Locate every blood parasite and identify its species.
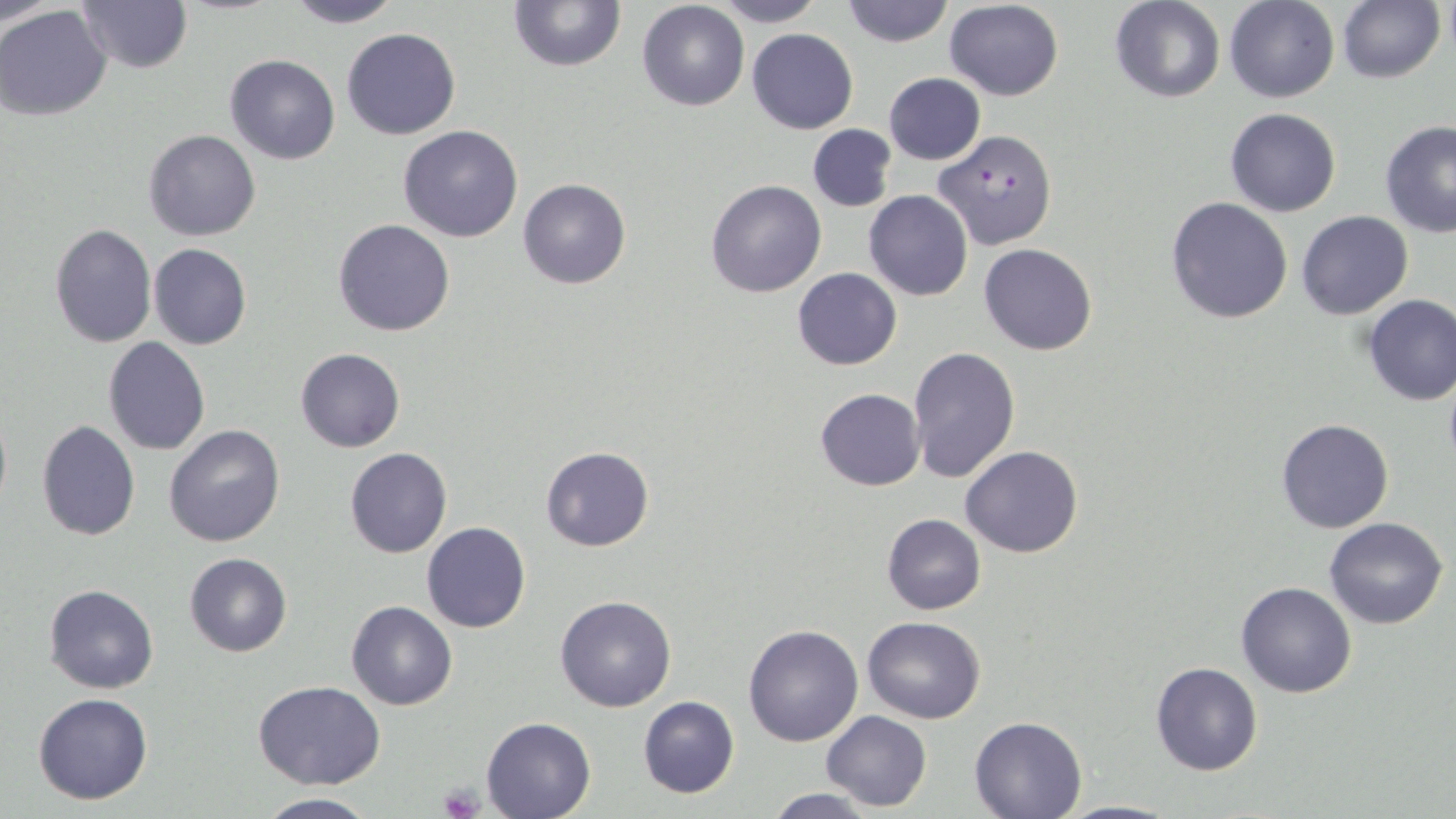

Approximate bounding boxes as named x1/y1/x2/y2 corners in pixels.
Plasmodium falciparum-infected red blood cells: (x1=934, y1=130, x2=1058, y2=249).
No Plasmodium ovale, Plasmodium malariae, Plasmodium vivax, Babesia divergens, or Trypanosoma brucei observed.

Summary:
  - Uninfected red blood cell locations: (x1=1, y1=0, x2=61, y2=29), (x1=280, y1=0, x2=404, y2=28), (x1=507, y1=0, x2=626, y2=71), (x1=712, y1=0, x2=824, y2=27), (x1=839, y1=0, x2=954, y2=48), (x1=1110, y1=0, x2=1224, y2=103), (x1=1225, y1=0, x2=1339, y2=102), (x1=77, y1=1, x2=193, y2=75), (x1=944, y1=1, x2=1063, y2=100), (x1=637, y1=2, x2=748, y2=112), (x1=1336, y1=2, x2=1445, y2=84), (x1=0, y1=5, x2=113, y2=122), (x1=341, y1=27, x2=460, y2=140), (x1=747, y1=28, x2=858, y2=132), (x1=224, y1=54, x2=340, y2=164), (x1=883, y1=72, x2=985, y2=164), (x1=1224, y1=107, x2=1342, y2=217), (x1=1379, y1=121, x2=1456, y2=238), (x1=807, y1=124, x2=897, y2=212), (x1=397, y1=125, x2=525, y2=242), (x1=142, y1=129, x2=263, y2=242), (x1=518, y1=178, x2=631, y2=289), (x1=705, y1=180, x2=825, y2=298), (x1=864, y1=190, x2=972, y2=301), (x1=1166, y1=197, x2=1293, y2=324), (x1=1298, y1=211, x2=1412, y2=320), (x1=334, y1=219, x2=455, y2=336), (x1=49, y1=224, x2=157, y2=347), (x1=149, y1=244, x2=252, y2=350), (x1=978, y1=244, x2=1097, y2=355), (x1=793, y1=267, x2=901, y2=369), (x1=1361, y1=294, x2=1456, y2=407), (x1=103, y1=337, x2=211, y2=455), (x1=906, y1=346, x2=1022, y2=484), (x1=294, y1=348, x2=406, y2=453), (x1=1443, y1=374, x2=1456, y2=477), (x1=814, y1=389, x2=924, y2=491), (x1=0, y1=402, x2=11, y2=520), (x1=1275, y1=417, x2=1394, y2=534), (x1=35, y1=420, x2=140, y2=540), (x1=165, y1=425, x2=285, y2=548), (x1=961, y1=445, x2=1083, y2=558), (x1=344, y1=447, x2=451, y2=559), (x1=540, y1=447, x2=655, y2=551), (x1=881, y1=513, x2=986, y2=615), (x1=1324, y1=517, x2=1448, y2=629), (x1=422, y1=522, x2=530, y2=633), (x1=185, y1=553, x2=292, y2=657), (x1=1235, y1=581, x2=1358, y2=698), (x1=44, y1=583, x2=160, y2=695), (x1=554, y1=595, x2=677, y2=713), (x1=347, y1=601, x2=457, y2=711), (x1=861, y1=615, x2=986, y2=724), (x1=742, y1=624, x2=863, y2=747), (x1=1150, y1=661, x2=1262, y2=776), (x1=252, y1=681, x2=386, y2=787), (x1=32, y1=693, x2=155, y2=805), (x1=637, y1=696, x2=739, y2=798), (x1=821, y1=710, x2=931, y2=811), (x1=970, y1=714, x2=1087, y2=817), (x1=481, y1=715, x2=597, y2=819), (x1=761, y1=787, x2=881, y2=819), (x1=253, y1=794, x2=382, y2=818), (x1=1056, y1=799, x2=1184, y2=818)
  - Platelet locations: (x1=437, y1=784, x2=483, y2=818)
  - Slide-level diagnosis: Plasmodium falciparum
  - Image size: 1456×819 pixels
  - Magnification: 1000x
  - Preparation: thin blood smear
  - Field of view: single
  - Stain: May-Grünwald-Giemsa
  - Modality: optical microscopy